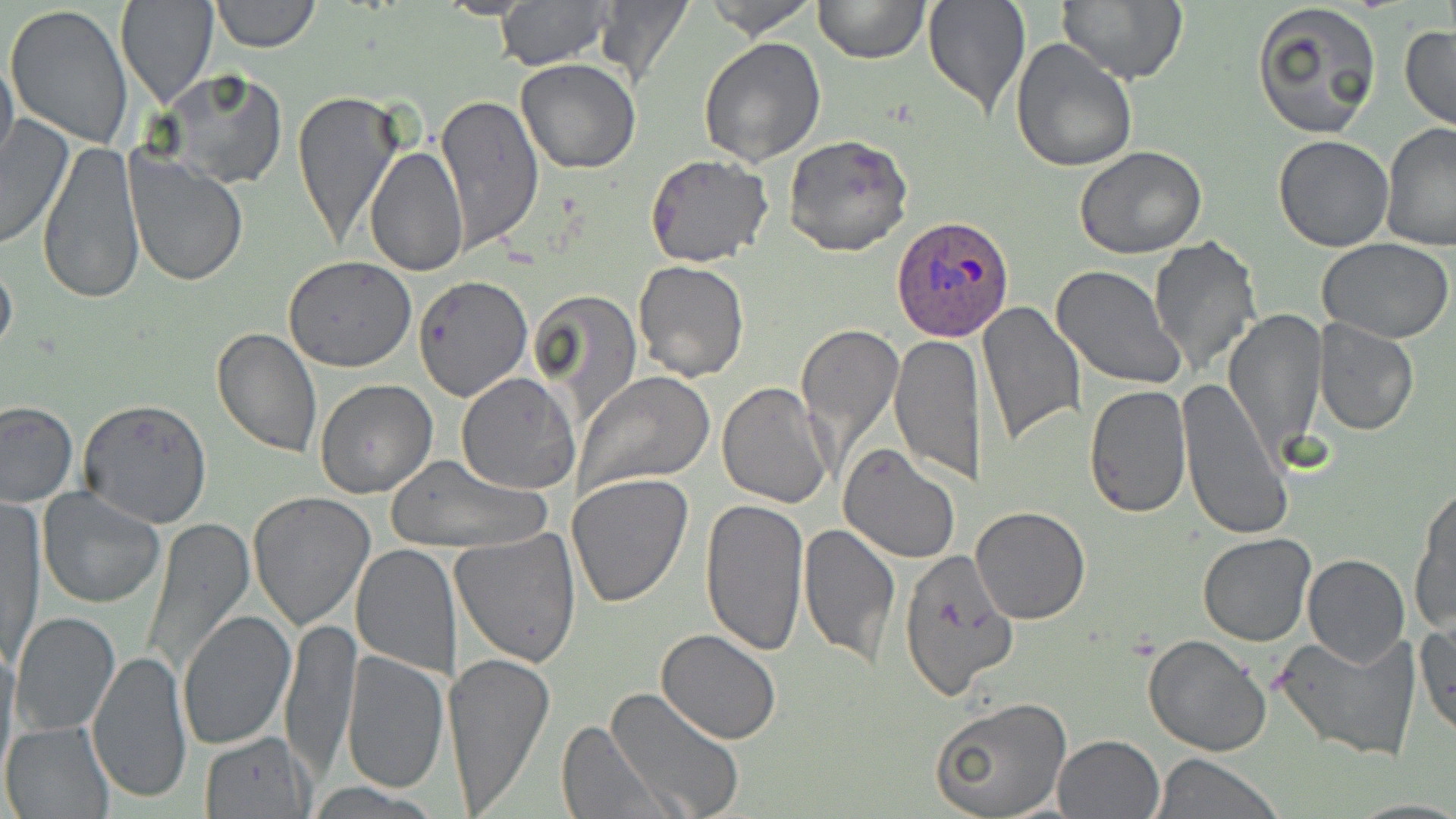

{
  "slide_level_diagnosis": "Plasmodium ovale",
  "magnification": "1000x",
  "modality": "light microscopy",
  "plasmodium_ovale_infected_red_blood_cell_locations": "approximate bounding boxes as [x1, y1, x2, y2] in pixels: [893, 215, 1014, 342]",
  "image_size": "1456×819 pixels",
  "preparation": "thin blood film",
  "field_of_view": "one of a larger specimen",
  "uninfected_red_blood_cell_locations": "approximate bounding boxes as [x1, y1, x2, y2] in pixels: [209, 0, 322, 53], [702, 0, 822, 40], [813, 0, 929, 64], [921, 0, 1031, 118], [1056, 0, 1187, 85], [1251, 0, 1382, 139], [116, 1, 216, 108], [495, 1, 612, 69], [591, 1, 696, 91], [5, 4, 133, 146], [1400, 24, 1456, 131], [1011, 36, 1139, 173], [698, 37, 827, 166], [0, 48, 19, 179], [515, 58, 640, 172], [157, 68, 286, 189], [292, 87, 404, 248], [436, 94, 543, 251], [0, 113, 76, 250], [1381, 123, 1456, 251], [784, 134, 913, 258], [1273, 135, 1395, 251], [38, 138, 145, 306], [365, 145, 469, 276], [1074, 147, 1206, 260], [124, 151, 248, 286], [645, 153, 773, 268], [1148, 234, 1262, 378], [1317, 237, 1453, 343], [0, 251, 18, 365], [284, 257, 417, 372], [633, 260, 748, 382], [1051, 264, 1187, 390], [415, 275, 532, 401], [530, 289, 644, 426], [976, 299, 1083, 447], [1225, 309, 1327, 456], [1314, 321, 1419, 435], [795, 322, 904, 463], [210, 327, 323, 460], [890, 335, 987, 484], [573, 371, 715, 495], [456, 372, 580, 493], [1174, 375, 1292, 541], [313, 380, 436, 499], [715, 380, 834, 508], [1083, 384, 1193, 518], [77, 398, 213, 528], [0, 400, 77, 506], [839, 445, 962, 565], [383, 454, 549, 554], [567, 474, 694, 610], [1410, 486, 1456, 634], [37, 488, 165, 609], [247, 490, 376, 630], [3, 499, 42, 668], [698, 500, 813, 656], [969, 506, 1090, 624], [142, 517, 253, 679], [797, 523, 899, 666], [451, 529, 583, 668], [1197, 533, 1316, 646], [351, 542, 460, 677], [896, 546, 1020, 700], [1302, 554, 1409, 668], [178, 609, 296, 750], [10, 611, 120, 737], [279, 617, 360, 776], [1415, 619, 1455, 739], [656, 629, 782, 745], [1271, 630, 1421, 763], [1144, 634, 1272, 756], [0, 638, 19, 780], [87, 647, 194, 804], [442, 649, 555, 814], [340, 651, 449, 793], [604, 686, 747, 819], [930, 695, 1072, 818], [1, 720, 114, 818], [555, 721, 672, 818], [199, 731, 314, 817], [1053, 733, 1163, 818], [1154, 753, 1281, 818], [306, 781, 443, 817]",
  "stain": "May-Grünwald-Giemsa"
}